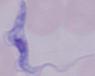
Photomicrograph. A trypanosome is seen. Captured at 1000x magnification.